Comment on the morphology of the erythrocytes.
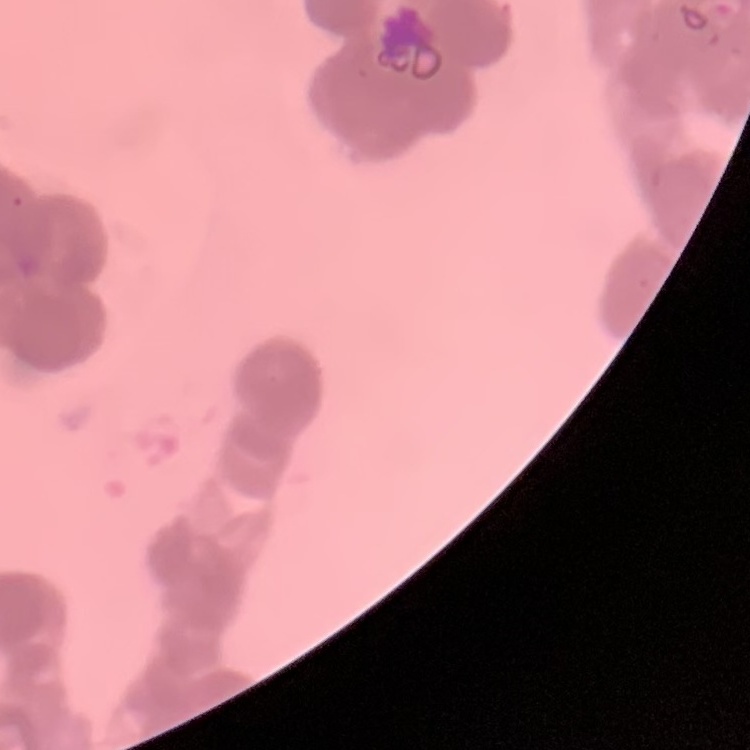

They show rouleaux formation.

Thin blood film. One tile cut from a larger photomicrograph. Field's or Giemsa stain.